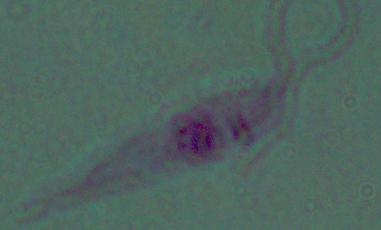
A Leishmania parasite is shown. Micrograph. Captured at 1000x magnification.